Comment on the morphology of the red blood cells.
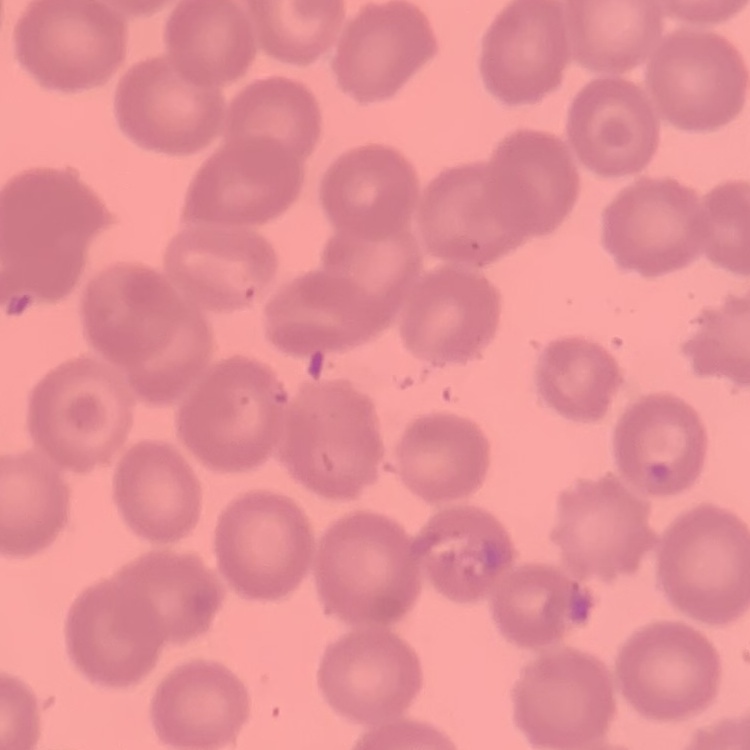

No rouleaux formation.

Summary:
  - Image type: one tile cut from a larger photomicrograph
  - Stain: Field's or Giemsa
  - Preparation: thin peripheral smear